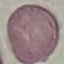
result = no malaria parasites detected
capture = smartphone camera at the microscope eyepiece
stain = Giemsa
image type = automatically extracted cell patch, resized to 64 × 64 pixels
preparation = thin blood smear